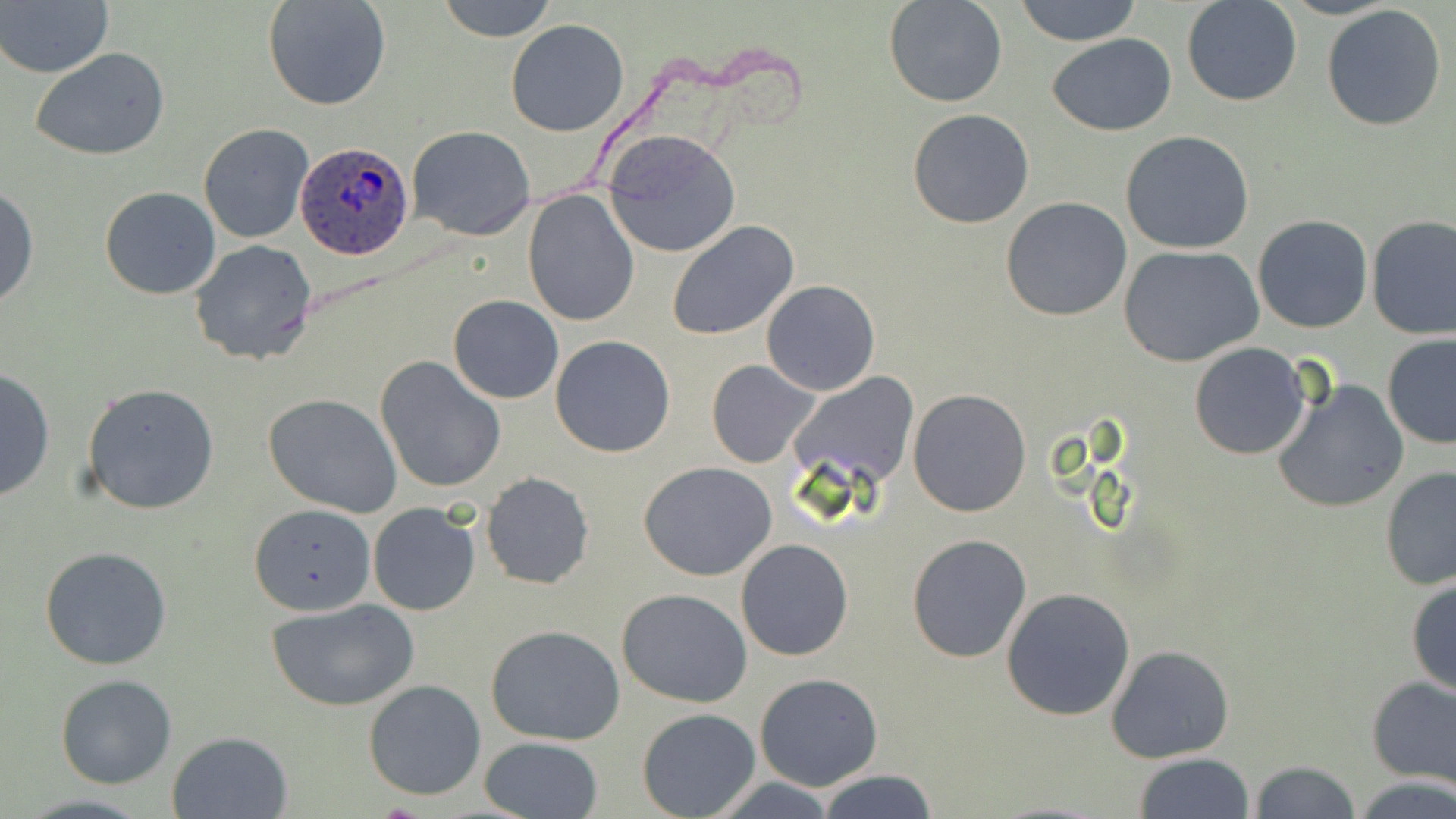 Approximate bounding boxes as [x1, y1, x2, y2] in pixels. Uninfected red blood cell locations: [1, 0, 116, 78], [262, 0, 392, 111], [434, 0, 560, 42], [883, 0, 1007, 107], [1012, 0, 1143, 46], [1181, 0, 1303, 107], [1320, 4, 1449, 133], [504, 20, 629, 136], [1046, 33, 1176, 136], [29, 47, 173, 163], [907, 109, 1035, 228], [198, 123, 314, 245], [407, 126, 535, 242], [604, 130, 740, 257], [1120, 130, 1255, 254], [0, 185, 38, 310], [100, 185, 221, 300], [521, 187, 639, 327], [1000, 197, 1132, 321], [1366, 214, 1456, 340], [1252, 215, 1373, 334], [667, 220, 799, 340], [189, 239, 318, 365], [1119, 245, 1264, 368], [762, 280, 879, 396], [447, 295, 563, 404], [1381, 334, 1456, 450], [551, 336, 677, 457], [1189, 343, 1312, 459], [375, 355, 507, 495], [706, 358, 822, 469], [0, 369, 55, 502], [794, 374, 919, 490], [1269, 377, 1410, 515], [83, 383, 220, 514], [907, 388, 1032, 517], [262, 393, 405, 517], [639, 461, 778, 580], [1379, 466, 1456, 593], [480, 472, 594, 589], [249, 502, 377, 615], [367, 503, 481, 615], [907, 533, 1033, 663], [736, 539, 853, 661], [39, 545, 172, 669], [1406, 575, 1456, 699], [616, 588, 752, 709], [1001, 588, 1135, 721], [268, 600, 419, 712], [485, 625, 627, 746], [1106, 643, 1235, 764], [55, 673, 178, 789], [754, 673, 884, 791], [1365, 675, 1456, 787], [364, 680, 485, 800], [637, 705, 760, 818], [167, 731, 293, 819], [476, 735, 603, 819], [1133, 753, 1257, 818], [1250, 760, 1363, 818], [816, 769, 940, 819], [1348, 774, 1456, 819], [706, 778, 844, 816], [14, 793, 156, 819]. Plasmodium ovale-infected red blood cell locations: [294, 143, 414, 261]. Slide-level diagnosis: Plasmodium ovale. May-Grünwald-Giemsa stain. Captured at 1000x magnification. Thin blood smear. Light microscopy. Image is 1456×819 pixels. Single field of view.